Locate every blood parasite and identify its species.
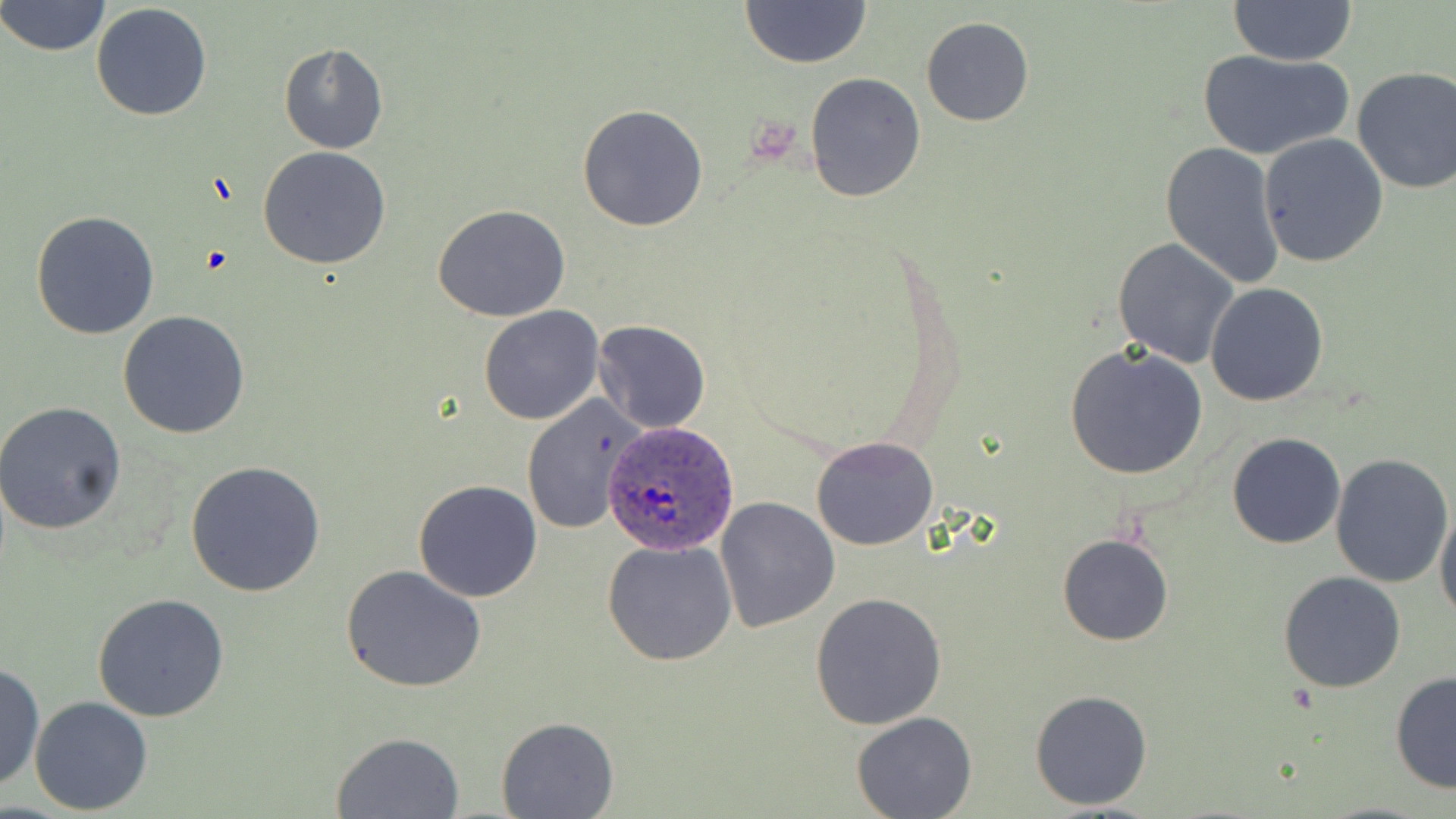
Approximate bounding boxes as [x1, y1, x2, y2] in pixels.
Plasmodium ovale-infected red blood cells: [606, 424, 736, 555].
No Plasmodium falciparum, Plasmodium malariae, Plasmodium vivax, Babesia divergens, or Trypanosoma brucei observed.

Summary:
  - Uninfected red blood cell locations: [1229, 0, 1358, 65], [0, 1, 112, 57], [740, 1, 873, 69], [91, 3, 214, 120], [921, 16, 1034, 126], [279, 43, 388, 153], [1197, 48, 1355, 161], [1351, 66, 1456, 196], [805, 72, 926, 204], [577, 103, 708, 232], [1258, 131, 1389, 268], [1160, 142, 1287, 291], [259, 146, 391, 268], [432, 204, 571, 321], [31, 209, 161, 340], [1113, 237, 1241, 369], [1205, 283, 1328, 406], [478, 305, 603, 426], [118, 310, 250, 438], [591, 320, 710, 435], [1064, 344, 1209, 481], [520, 394, 647, 534], [0, 403, 128, 535], [1227, 432, 1345, 548], [811, 436, 939, 551], [1225, 442, 1453, 568], [1331, 453, 1454, 588], [185, 459, 328, 597], [413, 480, 542, 602], [716, 496, 839, 632], [1435, 505, 1456, 627], [1057, 533, 1172, 646], [601, 537, 738, 668], [341, 564, 486, 692], [1278, 571, 1407, 693], [810, 590, 947, 729], [93, 594, 230, 722], [1, 661, 44, 794], [1390, 671, 1456, 795], [1028, 689, 1153, 811], [29, 695, 153, 816], [851, 712, 978, 819], [497, 715, 618, 817], [330, 731, 465, 818]
  - Slide-level diagnosis: Plasmodium ovale
  - Stain: May-Grünwald-Giemsa
  - Preparation: thin blood film
  - Modality: optical microscopy
  - Field of view: single
  - Magnification: 1000x
  - Image size: 1456×819 pixels